Report the malaria status of this cell.
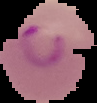

Parasitized.

Image is 97×103 pixels. From a thin blood smear. Segmented cell region on a black background.